Assess this cell for malaria.
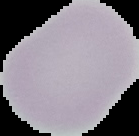
Uninfected.

Summary:
  - Image size: 139×136 pixels
  - Image type: segmented cell region on a black background
  - Preparation: thin blood smear